Assess the morphology of the red blood cells.
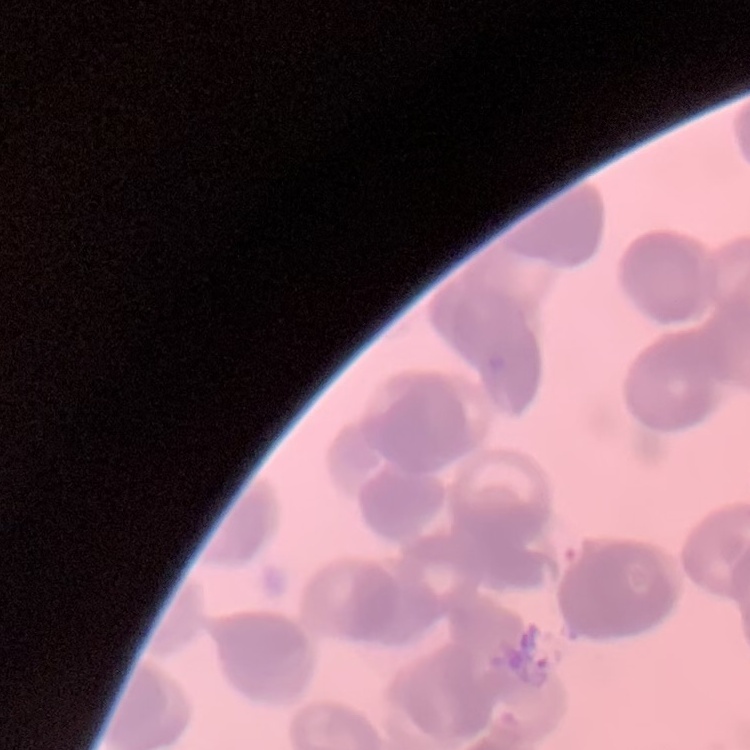

Rouleaux formation.

stain = Field's or Giemsa
image type = one tile cut from a larger photomicrograph
preparation = thin peripheral smear